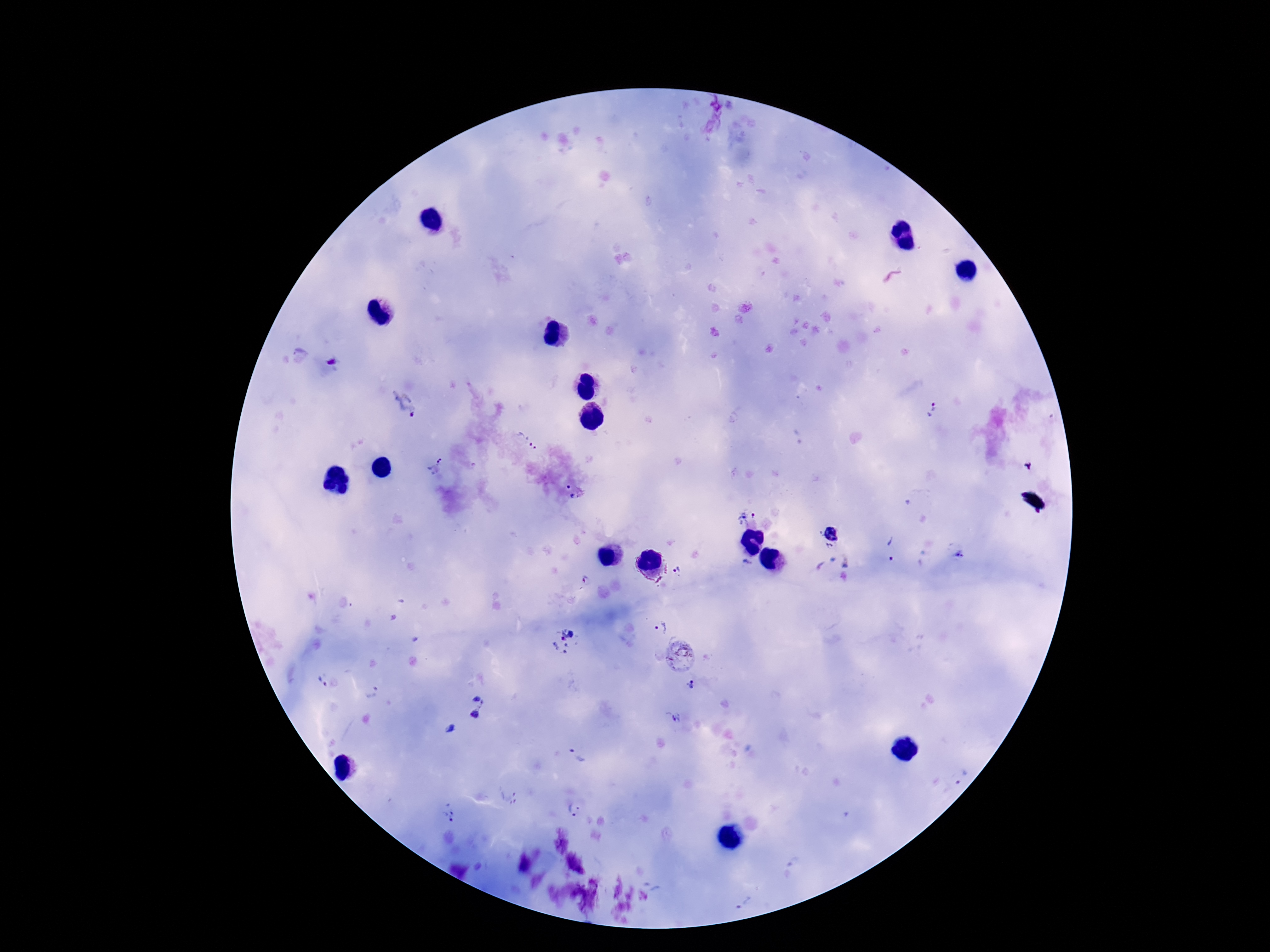
Approximate object centers, in pixels from the top-left corner. Plasmodium parasite locations: (x=713, y=116), (x=331, y=362), (x=404, y=403), (x=931, y=408), (x=527, y=439), (x=1027, y=466), (x=436, y=467), (x=569, y=487), (x=575, y=497), (x=746, y=513), (x=830, y=535), (x=890, y=549), (x=680, y=570), (x=585, y=582), (x=659, y=626), (x=565, y=640), (x=679, y=655), (x=321, y=682), (x=691, y=685), (x=373, y=693), (x=464, y=711), (x=676, y=719), (x=577, y=757), (x=960, y=773), (x=508, y=797), (x=573, y=809), (x=450, y=813), (x=743, y=899). Giemsa-stained preparation. Image is 1270×952 pixels. Thick blood film. Photographed through the microscope eyepiece with a smartphone camera. 100x magnification. Patient malaria status: positive. One field from this slide.